Give the position of every Plasmodium parasite.
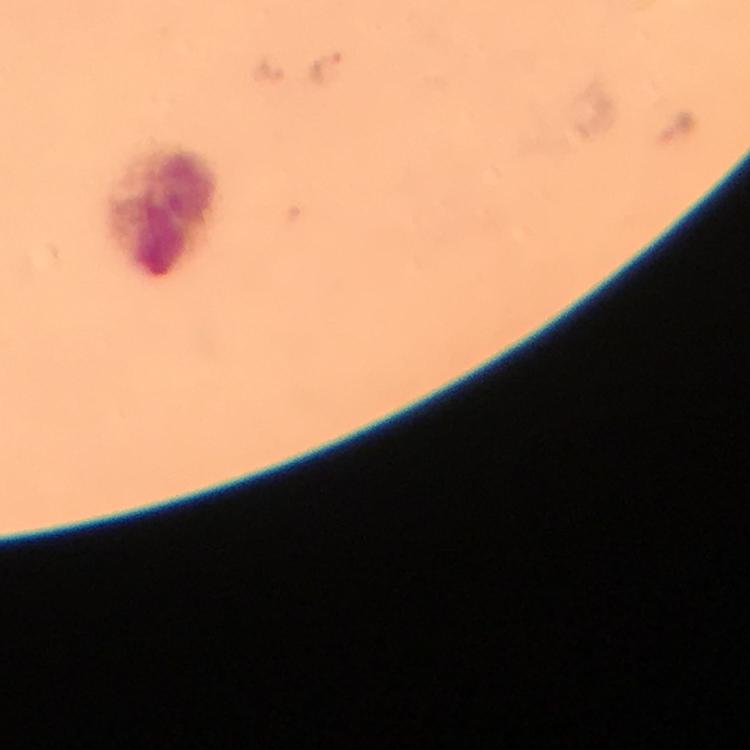

Approximate object centers, in pixels from the top-left corner.
Plasmodium parasites: (x=329, y=68).

Leukocyte locations: (x=164, y=214). Thick blood film. From a diagnostic examination for malaria. Immersion oil was used. At 100x magnification. Photographed through the microscope with a smartphone camera. Image is 750×750 pixels. A crop from one field of view. Giemsa stain.